Look for Plasmodium parasites.
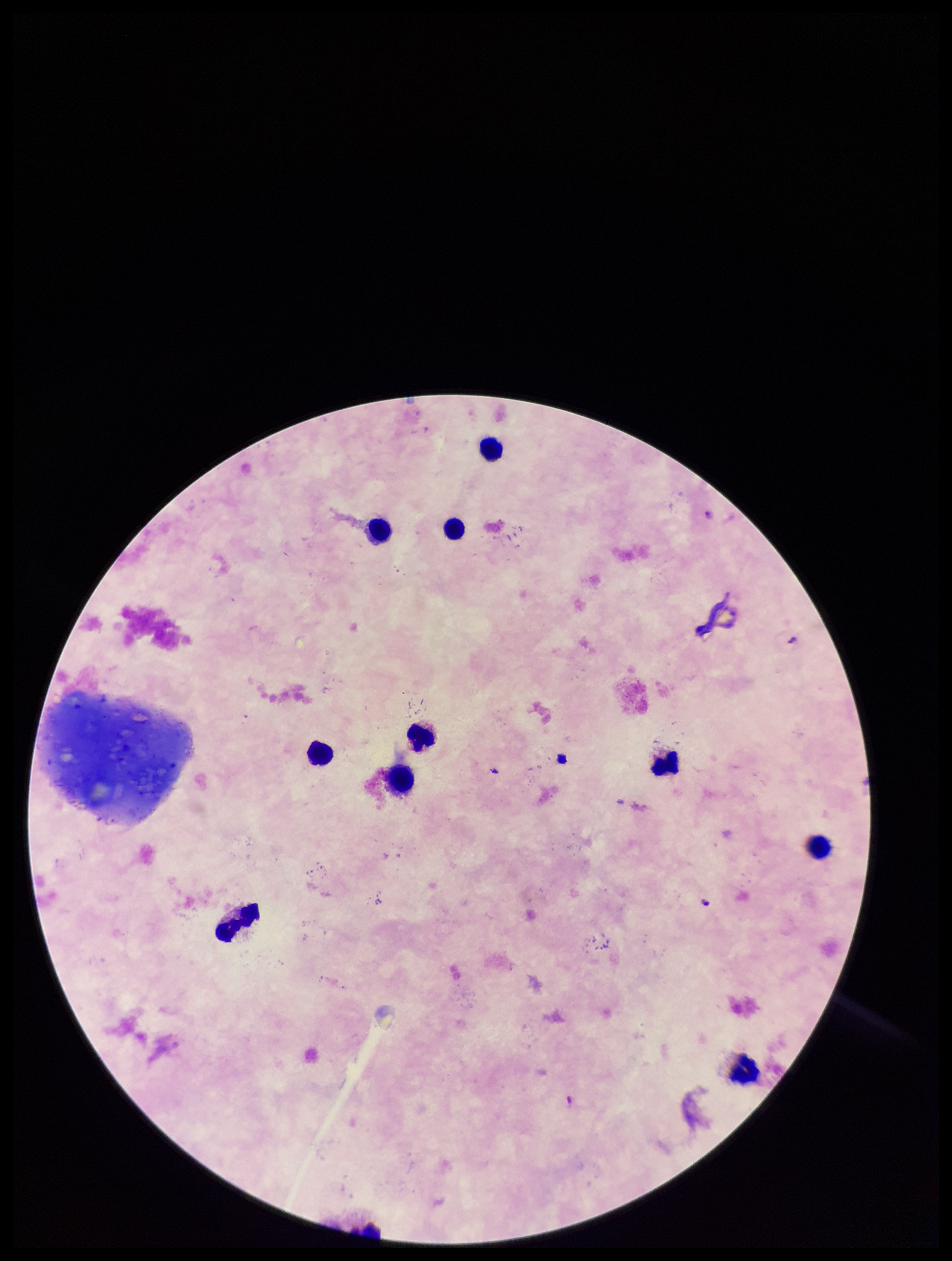
None seen.

Summary:
  - Field of view: single
  - Preparation: thick blood smear
  - Capture: smartphone photograph through the microscope eyepiece
  - Image size: 952×1261 pixels
  - Parasite count: 0
  - Patient malaria status: positive
  - Stain: Giemsa
  - Leukocyte count: 10
  - Species reported for this patient: Plasmodium falciparum